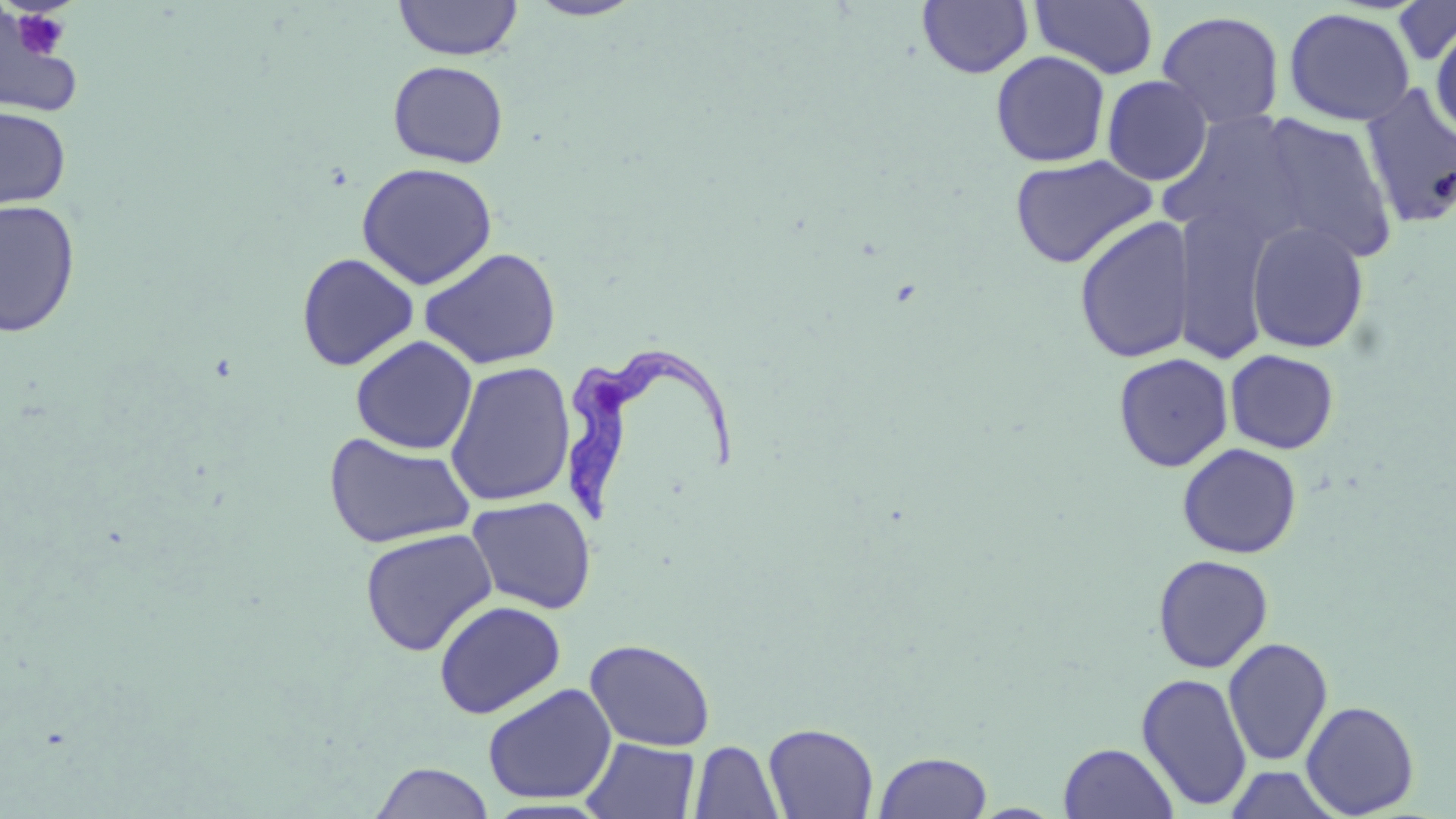

Summary:
  - Coordinate format: approximate bounding boxes as named x1/y1/x2/y2 corners in pixels
  - Platelet locations: (x1=10, y1=8, x2=74, y2=61)
  - Uninfected red blood cell locations: (x1=524, y1=0, x2=647, y2=21), (x1=1029, y1=0, x2=1159, y2=79), (x1=393, y1=1, x2=523, y2=61), (x1=917, y1=1, x2=1033, y2=79), (x1=1392, y1=1, x2=1456, y2=65), (x1=0, y1=6, x2=83, y2=120), (x1=1283, y1=7, x2=1415, y2=126), (x1=1156, y1=10, x2=1285, y2=129), (x1=1428, y1=17, x2=1456, y2=141), (x1=990, y1=50, x2=1111, y2=167), (x1=387, y1=61, x2=509, y2=168), (x1=1102, y1=75, x2=1212, y2=185), (x1=1359, y1=83, x2=1456, y2=229), (x1=0, y1=104, x2=71, y2=211), (x1=1158, y1=109, x2=1312, y2=249), (x1=1247, y1=114, x2=1399, y2=264), (x1=1009, y1=153, x2=1158, y2=269), (x1=356, y1=162, x2=498, y2=289), (x1=0, y1=199, x2=80, y2=337), (x1=1173, y1=203, x2=1277, y2=366), (x1=1073, y1=216, x2=1196, y2=364), (x1=1246, y1=221, x2=1369, y2=353), (x1=419, y1=247, x2=562, y2=370), (x1=295, y1=253, x2=419, y2=371), (x1=350, y1=335, x2=479, y2=455), (x1=1224, y1=349, x2=1339, y2=454), (x1=1112, y1=352, x2=1234, y2=473), (x1=445, y1=360, x2=576, y2=508), (x1=323, y1=431, x2=477, y2=549), (x1=1177, y1=443, x2=1302, y2=559), (x1=466, y1=496, x2=596, y2=614), (x1=359, y1=528, x2=498, y2=657), (x1=1152, y1=554, x2=1273, y2=673), (x1=433, y1=600, x2=566, y2=719), (x1=1223, y1=637, x2=1334, y2=766), (x1=585, y1=638, x2=716, y2=752), (x1=1135, y1=672, x2=1253, y2=811), (x1=482, y1=683, x2=617, y2=804), (x1=1300, y1=700, x2=1420, y2=817), (x1=763, y1=722, x2=879, y2=818), (x1=581, y1=736, x2=700, y2=819), (x1=689, y1=740, x2=784, y2=819), (x1=1058, y1=742, x2=1178, y2=819), (x1=874, y1=750, x2=993, y2=818), (x1=370, y1=761, x2=494, y2=819), (x1=1223, y1=764, x2=1343, y2=819)
  - Trypanosoma brucei locations: (x1=560, y1=352, x2=737, y2=529)
  - Slide-level diagnosis: Trypanosoma brucei
  - Image size: 1456×819 pixels
  - Preparation: thin blood film
  - Stain: May-Grünwald-Giemsa
  - Modality: light microscopy
  - Magnification: 1000x
  - Field of view: single